Describe the morphology of the red blood cells.
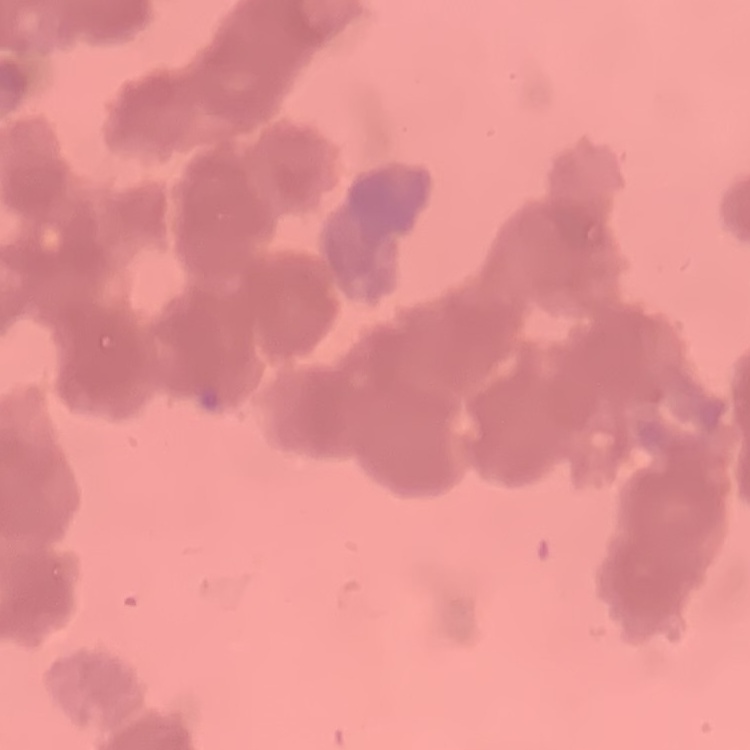
Rouleaux formation.

stain: Field's or Giemsa
image_type: square crop of a larger photomicrograph
preparation: thin peripheral smear